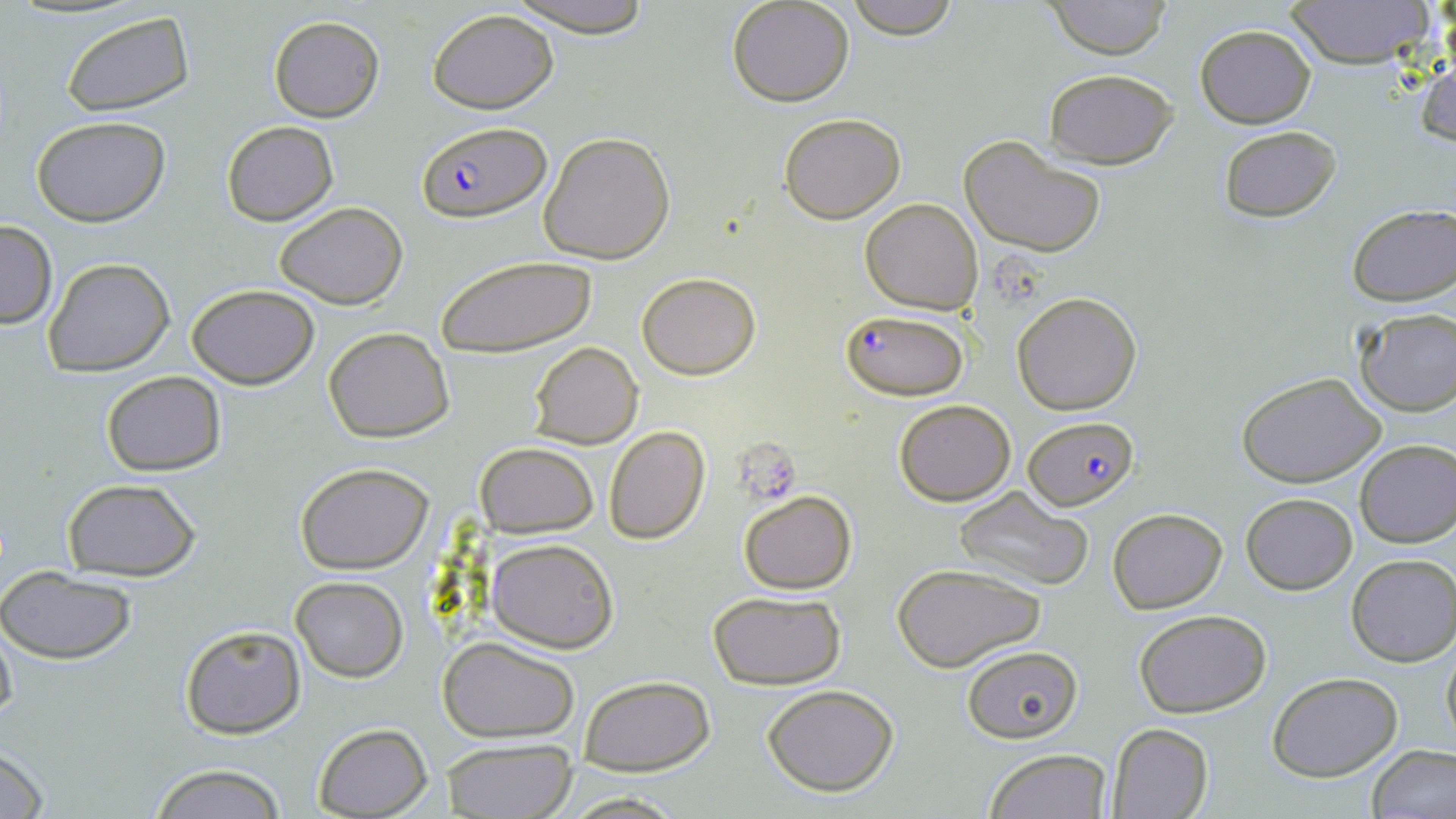
slide_level_diagnosis: Plasmodium falciparum
uninfected_red_blood_cell_locations: 'approximate bounding boxes as named x1/y1/x2/y2 corners in pixels: (x1=499, y1=0, x2=658, y2=35), (x1=725, y1=0, x2=856, y2=107), (x1=841, y1=0, x2=963, y2=38), (x1=1044, y1=0, x2=1173, y2=58), (x1=1285, y1=0, x2=1430, y2=70), (x1=429, y1=8, x2=559, y2=115), (x1=63, y1=11, x2=194, y2=118), (x1=268, y1=15, x2=384, y2=121), (x1=1194, y1=24, x2=1317, y2=128), (x1=1416, y1=46, x2=1456, y2=154), (x1=1043, y1=68, x2=1178, y2=168), (x1=778, y1=112, x2=906, y2=223), (x1=29, y1=115, x2=172, y2=225), (x1=221, y1=120, x2=337, y2=225), (x1=1217, y1=125, x2=1341, y2=222), (x1=539, y1=132, x2=675, y2=264), (x1=960, y1=136, x2=1106, y2=259), (x1=860, y1=198, x2=983, y2=315), (x1=275, y1=204, x2=406, y2=309), (x1=1345, y1=204, x2=1455, y2=307), (x1=0, y1=222, x2=56, y2=326), (x1=436, y1=253, x2=598, y2=357), (x1=42, y1=257, x2=175, y2=376), (x1=637, y1=272, x2=761, y2=379), (x1=187, y1=283, x2=318, y2=387), (x1=1011, y1=290, x2=1143, y2=414), (x1=1350, y1=306, x2=1455, y2=416), (x1=323, y1=327, x2=455, y2=443), (x1=528, y1=342, x2=642, y2=448), (x1=100, y1=370, x2=226, y2=476), (x1=1237, y1=370, x2=1386, y2=487), (x1=892, y1=398, x2=1018, y2=506), (x1=603, y1=424, x2=711, y2=544), (x1=1354, y1=439, x2=1455, y2=549), (x1=475, y1=440, x2=599, y2=538), (x1=294, y1=462, x2=433, y2=573), (x1=60, y1=478, x2=203, y2=582), (x1=953, y1=488, x2=1095, y2=592), (x1=737, y1=491, x2=856, y2=594), (x1=1240, y1=493, x2=1357, y2=594), (x1=1107, y1=506, x2=1228, y2=614), (x1=485, y1=537, x2=620, y2=653), (x1=1346, y1=553, x2=1456, y2=667), (x1=892, y1=564, x2=1044, y2=673), (x1=1, y1=568, x2=138, y2=665), (x1=291, y1=576, x2=408, y2=681), (x1=706, y1=590, x2=846, y2=691), (x1=1133, y1=609, x2=1271, y2=718), (x1=0, y1=620, x2=18, y2=734), (x1=179, y1=623, x2=306, y2=738), (x1=1441, y1=636, x2=1456, y2=754), (x1=437, y1=637, x2=581, y2=742), (x1=962, y1=644, x2=1083, y2=745), (x1=1267, y1=673, x2=1403, y2=781), (x1=577, y1=674, x2=715, y2=773), (x1=760, y1=683, x2=902, y2=796), (x1=311, y1=722, x2=435, y2=817), (x1=1106, y1=722, x2=1213, y2=819), (x1=440, y1=738, x2=578, y2=818), (x1=0, y1=744, x2=50, y2=819), (x1=1367, y1=744, x2=1456, y2=819), (x1=982, y1=747, x2=1113, y2=819), (x1=148, y1=765, x2=288, y2=819), (x1=558, y1=792, x2=690, y2=818)'
platelet_locations: 'approximate bounding boxes as named x1/y1/x2/y2 corners in pixels: (x1=734, y1=441, x2=802, y2=508)'
magnification: 1000x
field_of_view: one of a larger specimen
modality: light microscopy
plasmodium_falciparum_infected_red_blood_cell_locations: 'approximate bounding boxes as named x1/y1/x2/y2 corners in pixels: (x1=416, y1=122, x2=551, y2=222), (x1=841, y1=311, x2=966, y2=398), (x1=1025, y1=417, x2=1139, y2=510)'
stain: May-Grünwald-Giemsa
image_size: 1456×819 pixels
preparation: thin blood film